Assess the morphology of the erythrocytes.
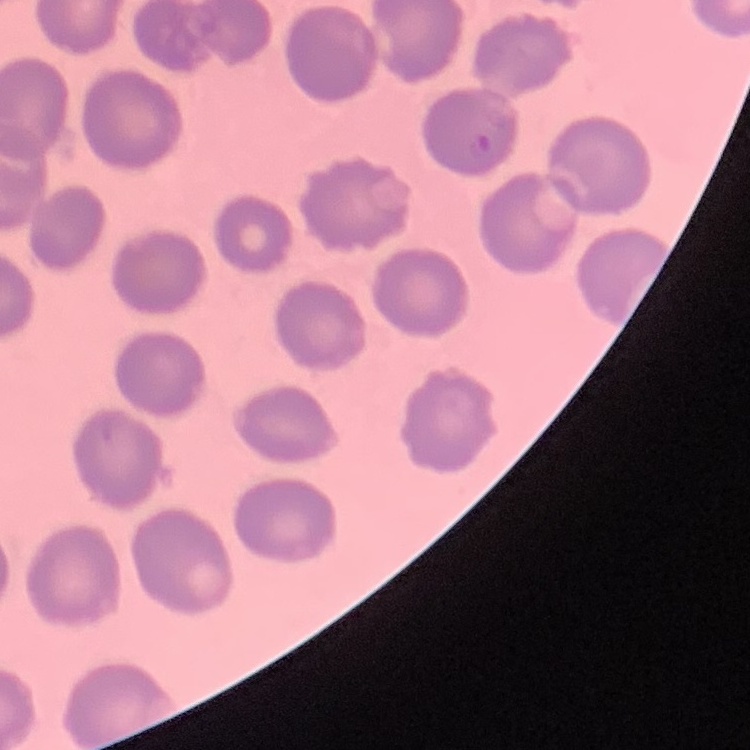

They show no rouleaux formation.

Summary:
  - Preparation: thin peripheral smear
  - Stain: Field's or Giemsa
  - Image type: one tile cut from a larger photomicrograph